Identify the parasite.
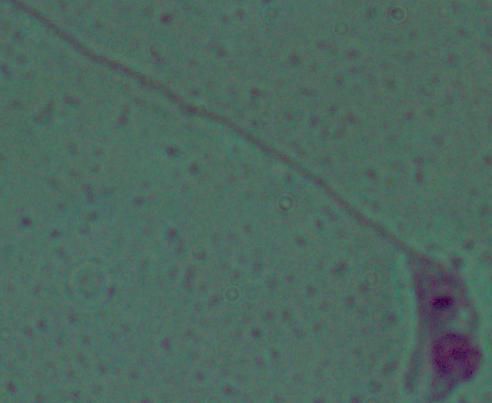
Leishmania.

1000x magnification. Micrograph.